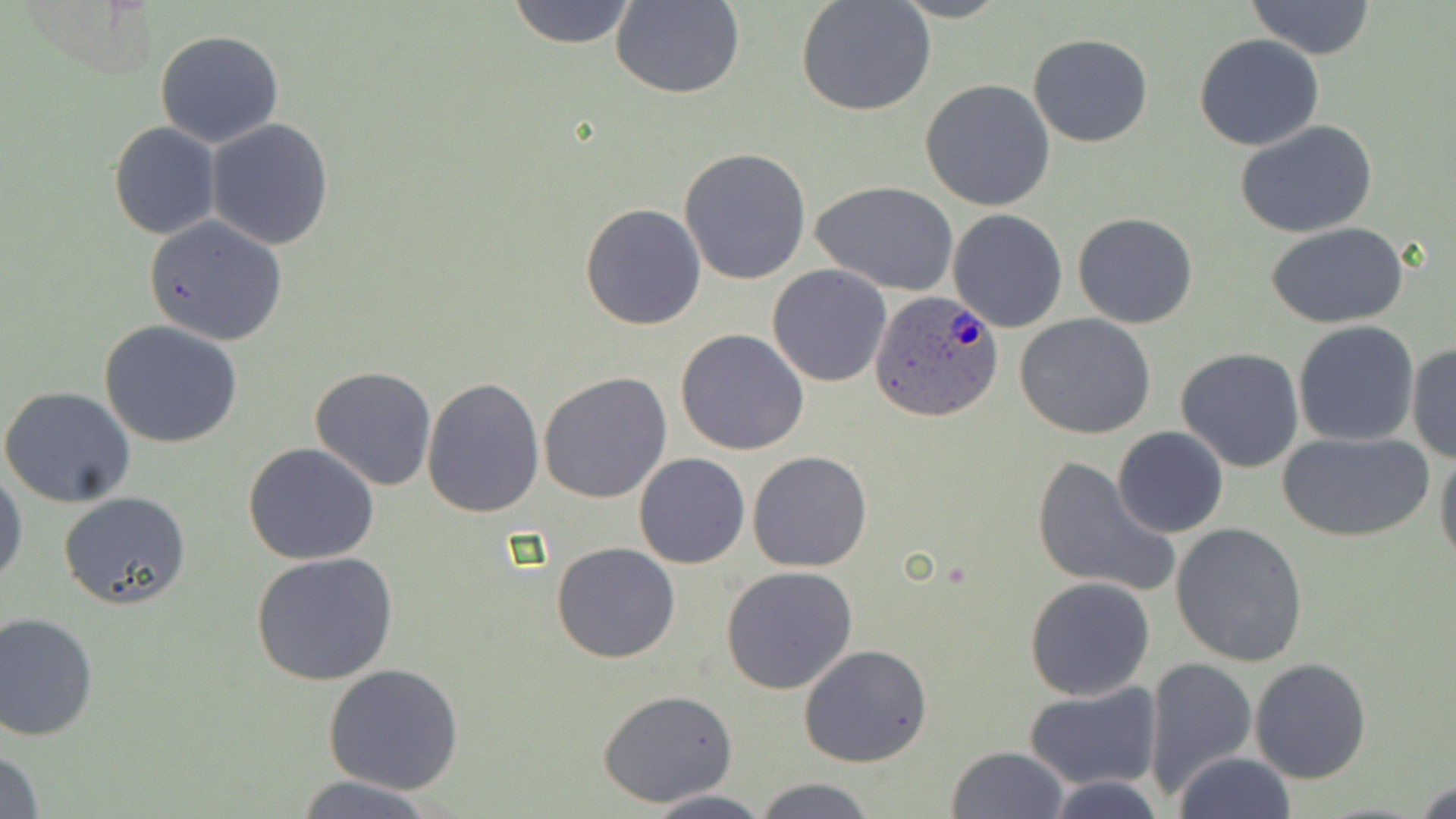
Summary:
  - Coordinate format: approximate bounding boxes as (x1, y1, x2, y2) in pixels
  - Uninfected red blood cell locations: (505, 0, 639, 49), (611, 0, 745, 99), (796, 0, 935, 117), (1245, 1, 1378, 59), (155, 30, 285, 148), (1028, 33, 1153, 148), (1194, 35, 1325, 151), (921, 80, 1055, 212), (205, 118, 335, 250), (108, 121, 223, 240), (1236, 121, 1379, 239), (679, 147, 814, 286), (813, 182, 959, 296), (579, 202, 706, 331), (948, 209, 1069, 333), (1073, 212, 1199, 329), (142, 216, 288, 346), (1265, 220, 1408, 328), (766, 265, 891, 388), (1013, 313, 1157, 440), (99, 320, 242, 449), (1291, 321, 1420, 447), (676, 329, 808, 456), (1406, 340, 1455, 464), (1175, 347, 1304, 472), (310, 367, 437, 492), (539, 372, 672, 504), (422, 378, 545, 519), (1, 386, 136, 508), (1113, 427, 1229, 539), (1277, 430, 1434, 544), (243, 442, 381, 566), (1435, 443, 1456, 568), (747, 451, 872, 571), (633, 453, 750, 570), (1031, 455, 1178, 598), (1, 470, 27, 589), (58, 490, 193, 610), (1170, 523, 1309, 668), (550, 543, 681, 663), (253, 553, 399, 689), (719, 566, 859, 695), (1024, 576, 1155, 701), (1, 611, 100, 741), (798, 644, 932, 768), (1141, 657, 1257, 802), (1248, 657, 1372, 784), (323, 664, 465, 794), (1024, 683, 1164, 794), (598, 690, 737, 807), (1, 743, 45, 819), (946, 745, 1068, 818), (1171, 751, 1297, 819), (287, 775, 445, 818), (1412, 775, 1455, 819), (1043, 776, 1171, 818), (752, 777, 878, 818), (643, 790, 778, 819)
  - Plasmodium ovale-infected red blood cell locations: (868, 289, 1006, 424)
  - Slide-level diagnosis: Plasmodium ovale
  - Modality: optical microscopy
  - Stain: May-Grünwald-Giemsa
  - Image size: 1456×819 pixels
  - Preparation: thin blood smear
  - Field of view: single
  - Magnification: 1000x